Assess this cell for malaria.
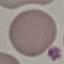

It is uninfected.

{
  "capture": "smartphone camera at the microscope eyepiece",
  "image_type": "cell patch, automatically extracted from a larger field of view and resized to 64 × 64 pixels",
  "preparation": "thin smear",
  "stain": "Giemsa"
}